Assess this cell for malaria.
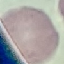

It is uninfected.

Giemsa-stained preparation. Photographed with a smartphone camera at the microscope eyepiece. Cell patch, automatically extracted from a larger field of view and resized to 64 × 64 pixels. Thin blood film.